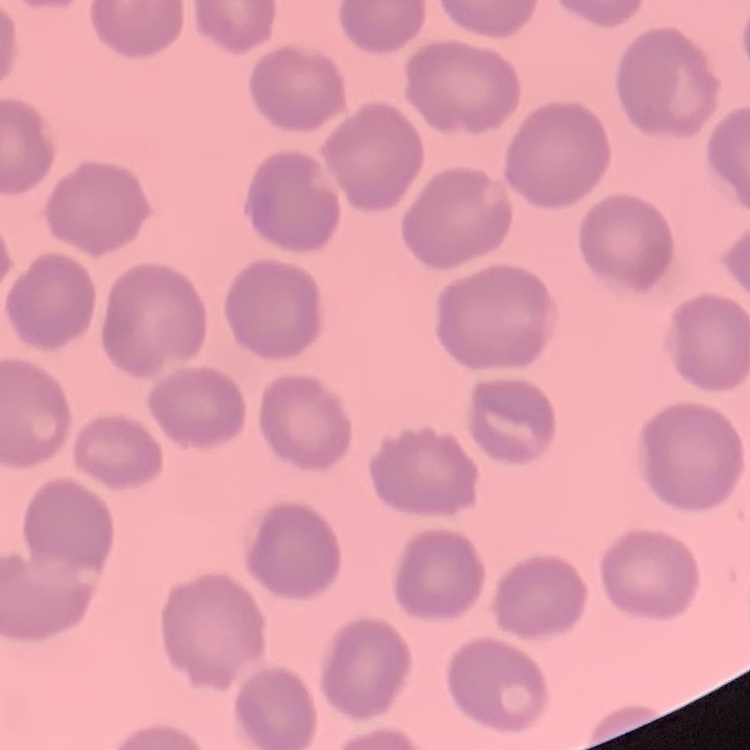
The red blood cells exhibit no rouleaux formation. One tile cut from a larger photomicrograph. Thin blood film. Field's or Giemsa stain.